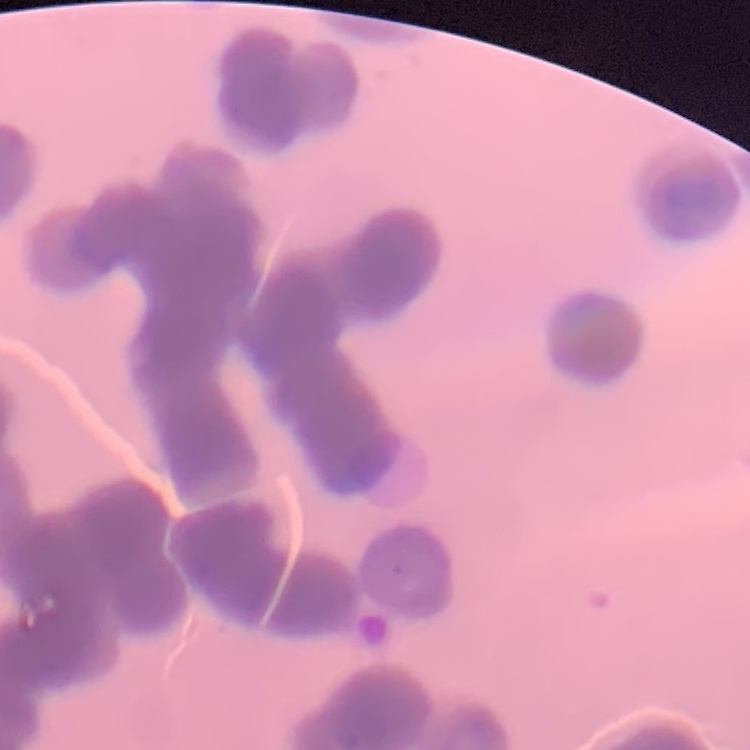
Summary:
  - Red blood cell morphology: rouleaux formation
  - Preparation: thin blood film
  - Stain: Field's or Giemsa
  - Image type: one tile cut from a larger photomicrograph